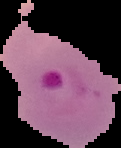

From a thin blood film. Image is 121×148 pixels. Segmented cell region on a black background. Malaria status: parasitized.